Locate platelets.
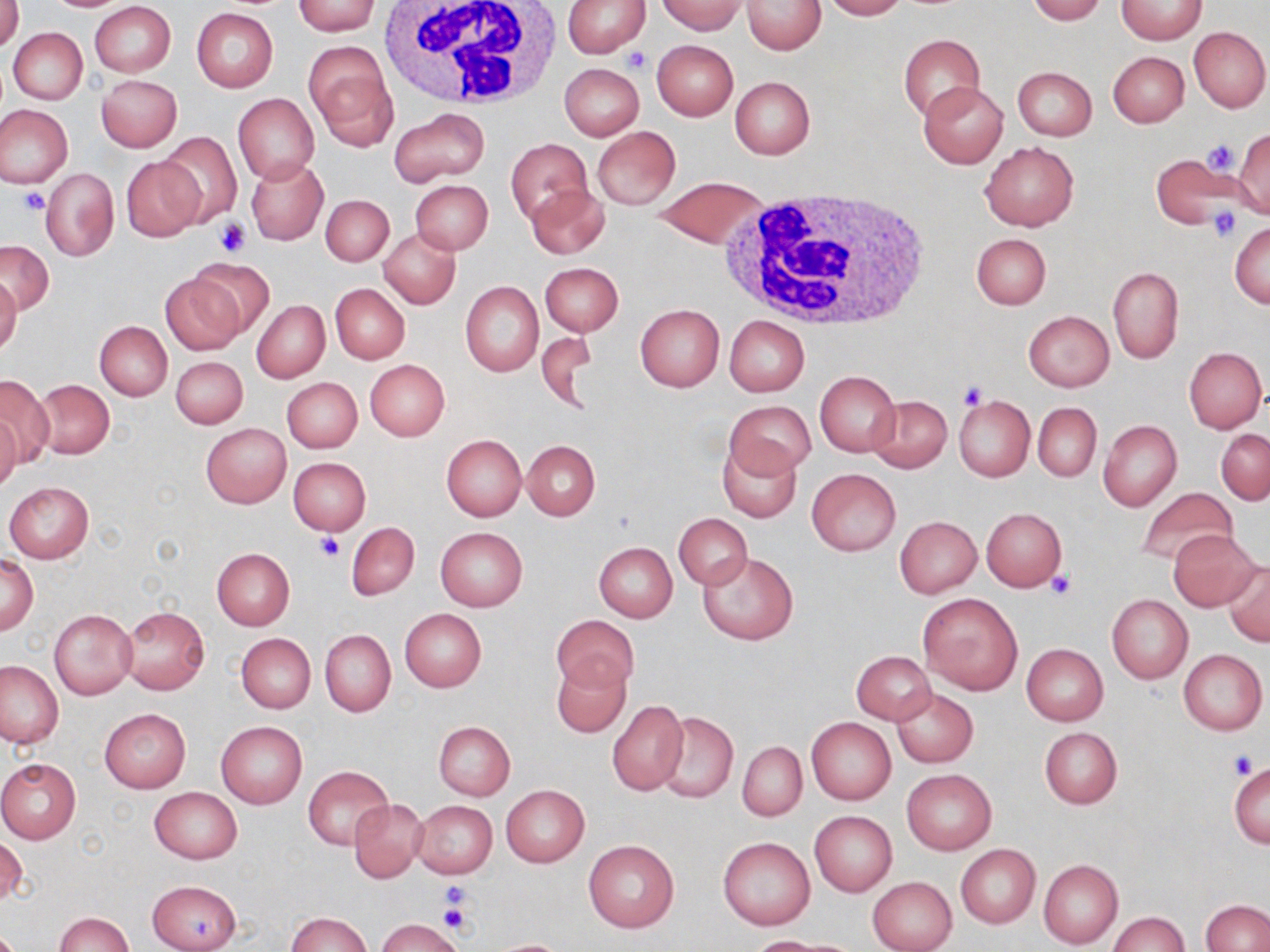

Approximate bounding boxes as named x1/y1/x2/y2 corners in pixels.
Platelets: (x1=624, y1=46, x2=653, y2=74), (x1=1202, y1=138, x2=1239, y2=174), (x1=18, y1=188, x2=51, y2=214), (x1=1207, y1=205, x2=1243, y2=242), (x1=216, y1=217, x2=250, y2=256), (x1=957, y1=381, x2=986, y2=409), (x1=315, y1=534, x2=344, y2=561), (x1=1045, y1=569, x2=1076, y2=601), (x1=1229, y1=751, x2=1259, y2=778), (x1=441, y1=884, x2=474, y2=918), (x1=438, y1=900, x2=473, y2=935).

{
  "slide_level_diagnosis": "no evidence of blood parasites",
  "preparation": "thin blood smear",
  "stain": "May-Grünwald-Giemsa",
  "magnification": "1000x",
  "image_size": "1270×952 pixels",
  "modality": "optical microscopy",
  "field_of_view": "one of a larger specimen",
  "uninfected_red_blood_cell_locations": "approximate bounding boxes as named x1/y1/x2/y2 corners in pixels: (x1=1, y1=0, x2=24, y2=52), (x1=562, y1=0, x2=650, y2=57), (x1=742, y1=0, x2=826, y2=54), (x1=820, y1=0, x2=907, y2=20), (x1=1026, y1=0, x2=1107, y2=24), (x1=89, y1=1, x2=176, y2=77), (x1=291, y1=1, x2=380, y2=35), (x1=655, y1=1, x2=746, y2=35), (x1=1116, y1=1, x2=1207, y2=43), (x1=191, y1=9, x2=278, y2=93), (x1=1189, y1=26, x2=1269, y2=112), (x1=8, y1=28, x2=88, y2=103), (x1=898, y1=34, x2=985, y2=119), (x1=652, y1=41, x2=738, y2=120), (x1=305, y1=42, x2=397, y2=151), (x1=1108, y1=51, x2=1188, y2=128), (x1=560, y1=63, x2=644, y2=141), (x1=1012, y1=65, x2=1097, y2=142), (x1=96, y1=74, x2=183, y2=152), (x1=730, y1=76, x2=815, y2=159), (x1=918, y1=82, x2=1007, y2=167), (x1=233, y1=93, x2=319, y2=184), (x1=0, y1=105, x2=73, y2=187), (x1=388, y1=107, x2=490, y2=187), (x1=592, y1=126, x2=680, y2=210), (x1=1232, y1=130, x2=1270, y2=214), (x1=158, y1=131, x2=242, y2=228), (x1=505, y1=138, x2=592, y2=228), (x1=981, y1=141, x2=1078, y2=230), (x1=1150, y1=152, x2=1238, y2=231), (x1=121, y1=154, x2=203, y2=241), (x1=246, y1=158, x2=327, y2=245), (x1=41, y1=167, x2=119, y2=261), (x1=654, y1=176, x2=767, y2=247), (x1=409, y1=179, x2=493, y2=255), (x1=526, y1=183, x2=610, y2=260), (x1=320, y1=194, x2=393, y2=266), (x1=1231, y1=222, x2=1270, y2=308), (x1=379, y1=229, x2=460, y2=310), (x1=972, y1=233, x2=1050, y2=311), (x1=1, y1=240, x2=53, y2=315), (x1=186, y1=258, x2=276, y2=340), (x1=540, y1=263, x2=623, y2=336), (x1=1108, y1=267, x2=1182, y2=363), (x1=160, y1=271, x2=244, y2=356), (x1=0, y1=273, x2=21, y2=357), (x1=460, y1=280, x2=544, y2=377), (x1=329, y1=283, x2=410, y2=364), (x1=252, y1=300, x2=329, y2=383), (x1=635, y1=305, x2=725, y2=391), (x1=1023, y1=310, x2=1114, y2=390), (x1=724, y1=315, x2=809, y2=397), (x1=94, y1=321, x2=172, y2=400), (x1=535, y1=330, x2=599, y2=409), (x1=1184, y1=347, x2=1266, y2=433), (x1=171, y1=356, x2=248, y2=429), (x1=364, y1=360, x2=449, y2=441), (x1=816, y1=372, x2=900, y2=455), (x1=0, y1=375, x2=54, y2=467), (x1=282, y1=377, x2=362, y2=454), (x1=33, y1=379, x2=115, y2=459), (x1=865, y1=395, x2=952, y2=473), (x1=953, y1=395, x2=1034, y2=482), (x1=725, y1=401, x2=814, y2=481), (x1=1033, y1=403, x2=1102, y2=482), (x1=0, y1=413, x2=21, y2=493), (x1=1098, y1=419, x2=1181, y2=510), (x1=200, y1=423, x2=290, y2=508), (x1=1216, y1=428, x2=1270, y2=505), (x1=441, y1=434, x2=527, y2=521), (x1=719, y1=438, x2=802, y2=522), (x1=522, y1=440, x2=600, y2=520), (x1=288, y1=457, x2=371, y2=535), (x1=807, y1=468, x2=900, y2=556), (x1=4, y1=482, x2=94, y2=563), (x1=1134, y1=486, x2=1238, y2=566), (x1=981, y1=507, x2=1068, y2=591), (x1=673, y1=513, x2=752, y2=590), (x1=894, y1=516, x2=981, y2=598), (x1=346, y1=522, x2=419, y2=601), (x1=435, y1=527, x2=527, y2=611), (x1=1168, y1=531, x2=1259, y2=610), (x1=593, y1=541, x2=678, y2=622), (x1=212, y1=548, x2=294, y2=629), (x1=698, y1=552, x2=798, y2=645), (x1=2, y1=555, x2=37, y2=634), (x1=1224, y1=560, x2=1270, y2=646), (x1=918, y1=592, x2=1024, y2=696), (x1=1107, y1=594, x2=1193, y2=683), (x1=119, y1=605, x2=209, y2=694), (x1=50, y1=609, x2=137, y2=700), (x1=400, y1=609, x2=486, y2=692), (x1=551, y1=614, x2=638, y2=691), (x1=320, y1=629, x2=395, y2=716), (x1=236, y1=632, x2=315, y2=713), (x1=1021, y1=643, x2=1108, y2=725), (x1=1179, y1=649, x2=1267, y2=735), (x1=851, y1=650, x2=935, y2=725), (x1=551, y1=657, x2=631, y2=738), (x1=0, y1=660, x2=65, y2=748), (x1=892, y1=688, x2=978, y2=768), (x1=607, y1=700, x2=689, y2=797), (x1=99, y1=708, x2=190, y2=793), (x1=656, y1=713, x2=738, y2=802), (x1=807, y1=717, x2=896, y2=805), (x1=216, y1=721, x2=307, y2=809), (x1=432, y1=721, x2=515, y2=800), (x1=1039, y1=727, x2=1122, y2=808), (x1=738, y1=742, x2=806, y2=821), (x1=0, y1=758, x2=81, y2=843), (x1=1229, y1=762, x2=1269, y2=847), (x1=304, y1=766, x2=392, y2=849), (x1=902, y1=770, x2=996, y2=854), (x1=500, y1=785, x2=589, y2=868), (x1=149, y1=786, x2=241, y2=864), (x1=348, y1=797, x2=428, y2=883), (x1=412, y1=801, x2=497, y2=879), (x1=809, y1=811, x2=896, y2=895), (x1=0, y1=835, x2=28, y2=906), (x1=718, y1=837, x2=814, y2=930), (x1=583, y1=839, x2=680, y2=932), (x1=956, y1=845, x2=1040, y2=927), (x1=1038, y1=860, x2=1123, y2=947), (x1=867, y1=876, x2=957, y2=952), (x1=147, y1=880, x2=241, y2=952), (x1=1202, y1=900, x2=1268, y2=952), (x1=1107, y1=911, x2=1189, y2=951), (x1=55, y1=912, x2=133, y2=952), (x1=286, y1=912, x2=370, y2=952), (x1=376, y1=918, x2=465, y2=952), (x1=747, y1=935, x2=830, y2=951), (x1=490, y1=938, x2=573, y2=952)",
  "white_blood_cell_locations": "approximate bounding boxes as named x1/y1/x2/y2 corners in pixels: (x1=375, y1=0, x2=565, y2=114), (x1=718, y1=189, x2=931, y2=327)"
}